Locate and identify every blood parasite.
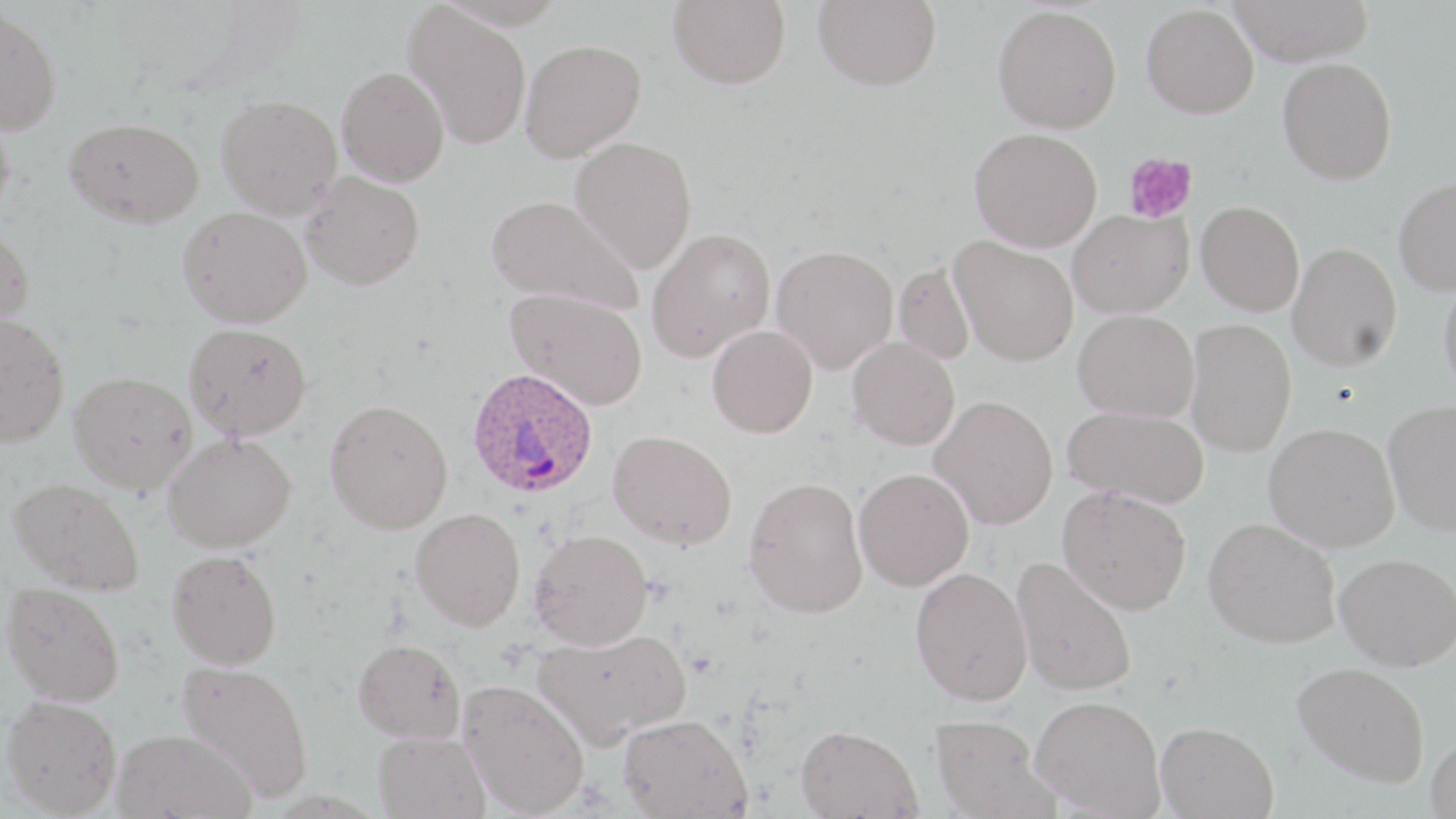

Approximate bounding boxes as (x1,y1)-(x2,y2) corner pairs in pixels.
Plasmodium ovale-infected red blood cells: (465,367)-(599,499).
No Plasmodium falciparum, Plasmodium malariae, Plasmodium vivax, Babesia divergens, or Trypanosoma brucei observed.

Platelet locations: (1123,152)-(1198,224). Uninfected red blood cell locations: (668,0)-(791,88), (813,0)-(942,90), (1228,0)-(1376,65), (403,2)-(533,149), (1141,3)-(1259,118), (0,4)-(62,135), (993,5)-(1122,133), (519,39)-(646,162), (1277,57)-(1397,184), (337,66)-(449,187), (217,95)-(343,219), (0,102)-(16,229), (64,117)-(204,228), (969,128)-(1102,252), (571,135)-(697,272), (300,171)-(425,290), (1393,176)-(1456,295), (486,194)-(642,314), (1196,200)-(1304,315), (178,206)-(312,327), (1067,208)-(1194,317), (0,224)-(35,333), (646,227)-(775,362), (950,237)-(1079,366), (1287,242)-(1402,371), (770,244)-(898,373), (894,261)-(975,365), (1438,272)-(1456,397), (505,287)-(648,410), (1073,310)-(1199,421), (0,313)-(70,446), (1185,318)-(1297,456), (184,323)-(312,439), (707,325)-(818,438), (848,337)-(960,450), (68,371)-(197,494), (930,394)-(1058,529), (324,398)-(454,534), (1383,399)-(1456,535), (1062,405)-(1209,509), (1264,422)-(1399,551), (608,429)-(737,549), (163,432)-(296,553), (853,468)-(974,591), (9,476)-(145,595), (743,476)-(868,618), (1058,486)-(1191,614), (410,508)-(526,631), (1204,517)-(1341,647), (529,529)-(654,650), (167,550)-(282,669), (1334,552)-(1456,670), (1011,557)-(1138,696), (910,566)-(1032,705), (3,582)-(124,706), (532,629)-(692,750), (353,638)-(465,742), (176,660)-(314,802), (1292,661)-(1430,787), (458,678)-(590,816), (2,694)-(122,816), (1030,695)-(1165,817), (619,714)-(751,818), (930,715)-(1055,819), (1155,721)-(1279,818), (795,724)-(923,818), (113,729)-(255,819), (373,731)-(489,819), (1426,733)-(1456,818). Slide-level diagnosis: Plasmodium ovale. May-Grünwald-Giemsa-stained preparation. Captured at 1000x magnification. Thin blood smear. Single field of view. Image is 1456×819 pixels. Light microscopy.